Assess this cell for malaria.
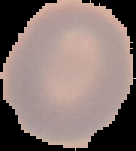
It is uninfected.

From a thin blood smear. Image is 136×151 pixels. Cell region segmented out of the field of view; the surrounding area is masked to black.